Name the parasite shown.
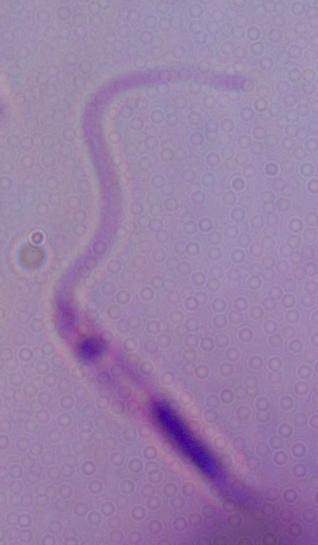

This is Leishmania.

Micrograph. 1000x magnification.